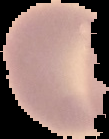
Summary:
  - Preparation: thin blood film
  - Image size: 109×139 pixels
  - Result: no malaria parasites seen
  - Image type: cell region segmented out of the field of view; surrounding area masked to black